Locate Plasmodium parasites and leukocytes.
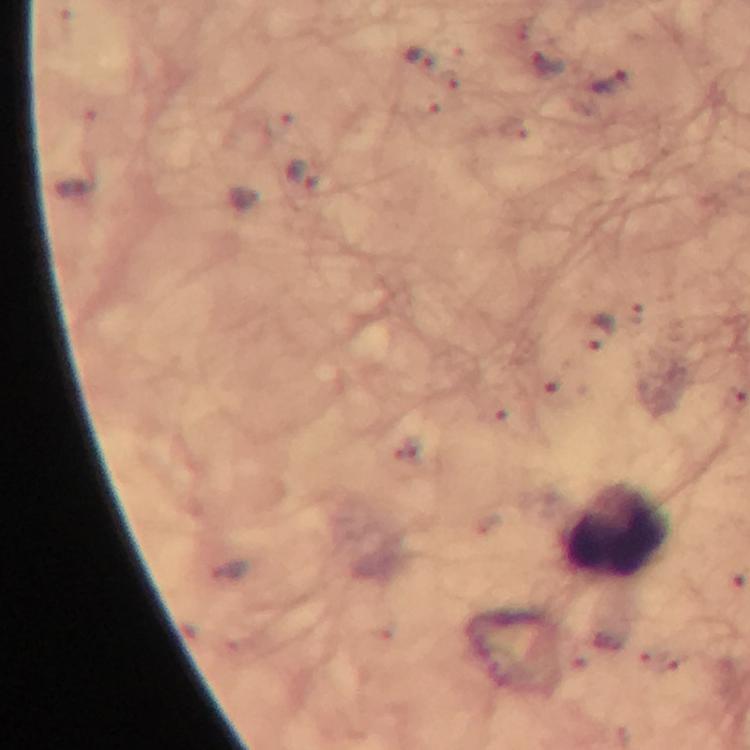

Approximate centers as {x, y} in pixels.
Plasmodium parasites: {419, 60}, {547, 67}, {612, 86}, {306, 176}, {597, 335}.
Leukocytes: {617, 530}.

A crop from one field of view. Smartphone photograph taken through a microscope. Giemsa stain. Thick smear. Image is 750×750 pixels. At 100x magnification. Immersion oil applied. From a malaria diagnostic workup.